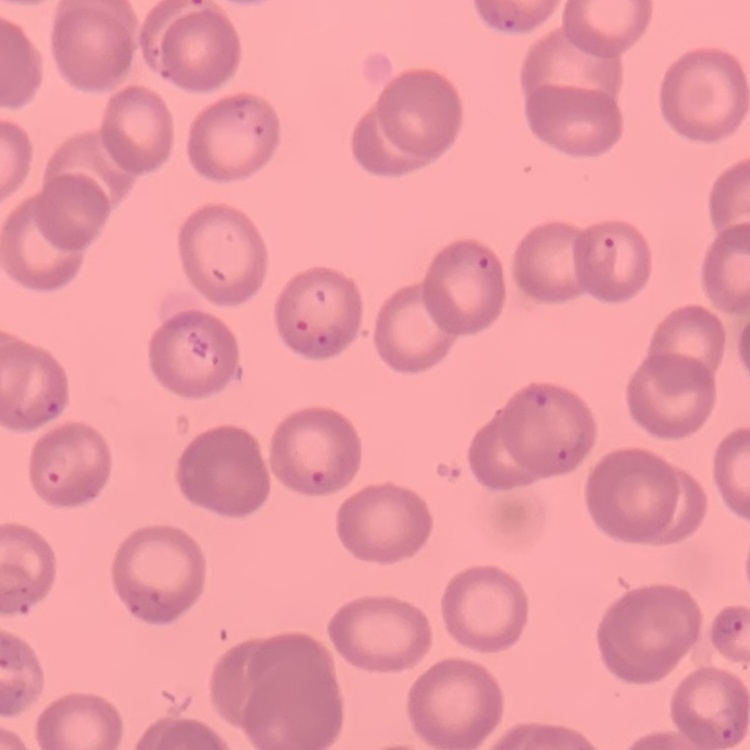
Summary:
  - Erythrocyte morphology: no rouleaux formation
  - Stain: Field's or Giemsa
  - Image type: one tile cut from a larger photomicrograph
  - Preparation: thin blood smear